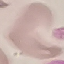
Summary:
  - Result: no malaria parasites detected
  - Stain: Giemsa
  - Preparation: thin blood film
  - Capture: smartphone camera at the microscope eyepiece
  - Image type: automatically extracted cell patch, resized to 64 × 64 pixels